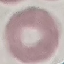

Summary:
  - Malaria status: uninfected
  - Preparation: thin blood smear
  - Image type: automatically extracted cell patch, resized to 64 × 64 pixels
  - Capture: smartphone through the microscope eyepiece
  - Stain: Giemsa